Describe the morphology of the erythrocytes.
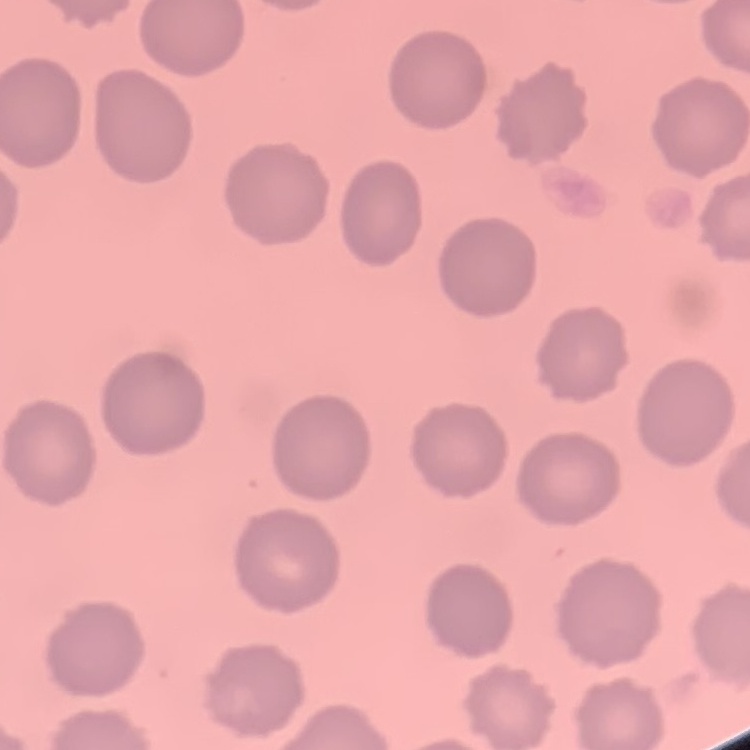

They show no rouleaux formation.

Summary:
  - Image type: square crop of a larger photomicrograph
  - Stain: Field's or Giemsa
  - Preparation: thin blood film